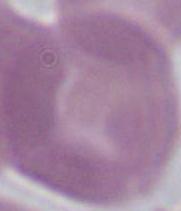
Micrograph. A red blood cell is seen. Captured at 1000x magnification.